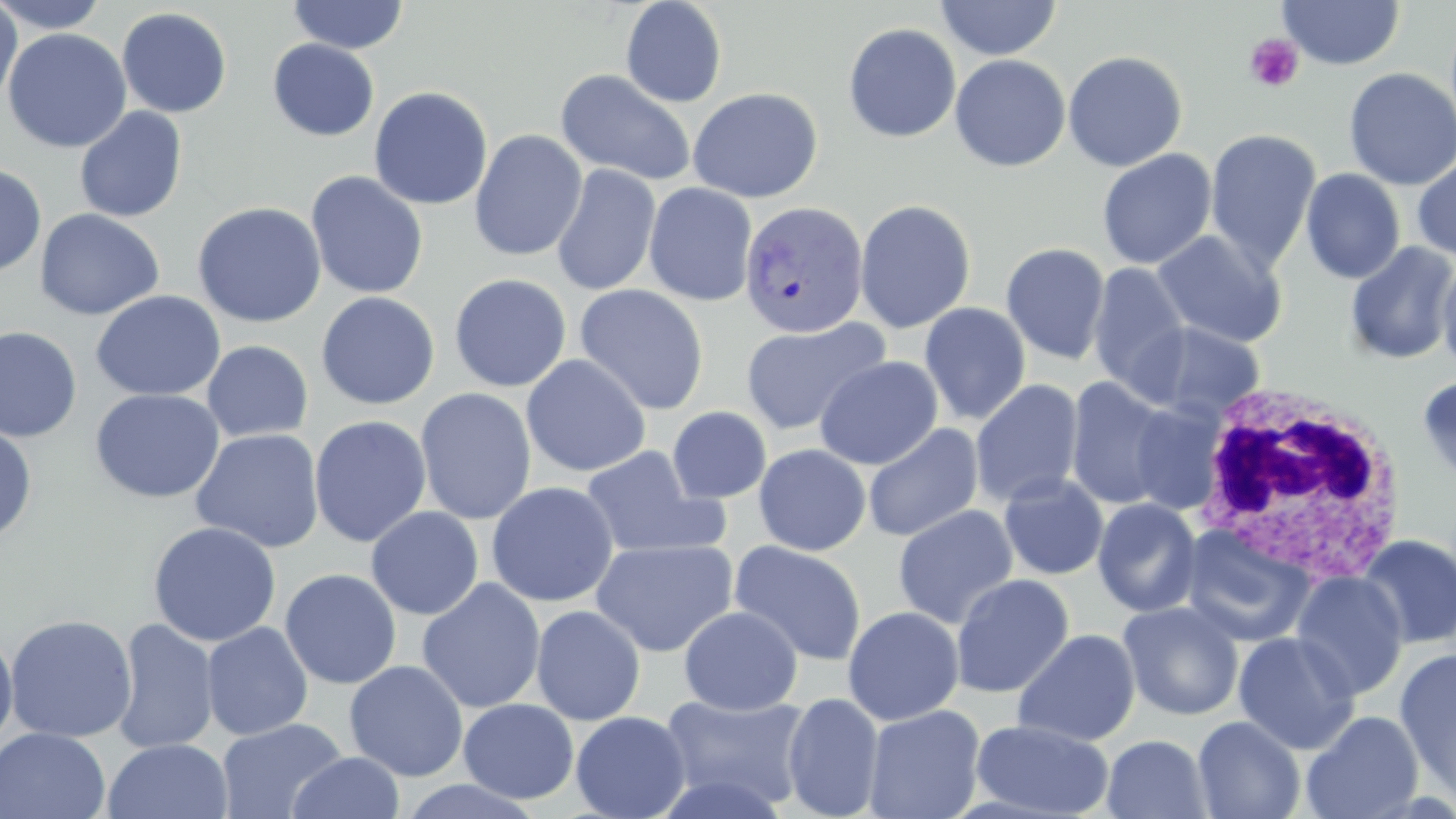

slide-level diagnosis = Plasmodium vivax
magnification = 1000x
image size = 1456×819 pixels
field of view = one of a larger specimen
white blood cell locations = approximate bounding boxes as (x1, y1, x2, y2) in pixels: (1189, 383, 1411, 580)
modality = light microscopy
Plasmodium vivax-infected red blood cell locations = approximate bounding boxes as (x1, y1, x2, y2) in pixels: (740, 202, 870, 339)
stain = May-Grünwald-Giemsa
platelet locations = approximate bounding boxes as (x1, y1, x2, y2) in pixels: (1244, 33, 1304, 93)
uninfected red blood cell locations = approximate bounding boxes as (x1, y1, x2, y2) in pixels: (0, 0, 110, 34), (287, 0, 409, 54), (620, 0, 727, 108), (1277, 0, 1405, 70), (935, 1, 1062, 60), (0, 2, 22, 110), (116, 7, 232, 118), (842, 23, 961, 143), (2, 28, 132, 153), (267, 39, 380, 141), (1063, 50, 1188, 172), (950, 54, 1071, 173), (1343, 67, 1456, 190), (555, 69, 697, 187), (369, 86, 493, 210), (687, 87, 823, 203), (74, 107, 188, 223), (1205, 128, 1321, 271), (469, 129, 588, 261), (1097, 149, 1217, 269), (1412, 154, 1456, 261), (0, 161, 47, 278), (551, 164, 661, 297), (1300, 169, 1405, 284), (305, 170, 429, 300), (643, 182, 757, 306), (854, 199, 976, 334), (192, 201, 327, 328), (34, 208, 164, 320), (1152, 230, 1288, 348), (1000, 242, 1111, 364), (1346, 242, 1456, 365), (1437, 254, 1456, 378), (1088, 263, 1190, 396), (449, 273, 572, 392), (574, 284, 709, 415), (90, 290, 226, 402), (316, 291, 440, 410), (919, 302, 1031, 425), (740, 317, 890, 435), (1133, 321, 1266, 421), (0, 325, 82, 443), (201, 340, 314, 443), (520, 354, 651, 477), (814, 355, 943, 470), (1416, 374, 1456, 486), (1066, 377, 1179, 510), (970, 379, 1084, 508), (415, 387, 537, 525), (90, 388, 225, 503), (1129, 402, 1226, 513), (667, 406, 772, 504), (309, 415, 432, 548), (862, 423, 983, 542), (0, 424, 38, 545), (191, 428, 325, 553), (753, 443, 871, 556), (579, 444, 726, 560), (998, 473, 1109, 580), (485, 482, 619, 607), (1093, 497, 1203, 618), (892, 505, 1019, 629), (365, 506, 484, 620), (147, 521, 282, 647), (1180, 523, 1316, 648), (1356, 535, 1456, 649), (590, 537, 739, 657), (729, 540, 867, 666), (280, 568, 402, 689), (1290, 571, 1409, 701), (951, 573, 1074, 698), (417, 578, 546, 714), (1118, 601, 1244, 720), (530, 605, 646, 726), (678, 605, 802, 715), (842, 606, 965, 726), (4, 614, 138, 744), (111, 618, 219, 754), (201, 622, 313, 740), (0, 628, 18, 752), (1012, 629, 1140, 746), (1232, 632, 1361, 754), (1395, 647, 1456, 798), (344, 660, 469, 781), (658, 691, 813, 813), (782, 693, 885, 818), (458, 698, 580, 804), (863, 704, 986, 819), (1301, 710, 1424, 819), (570, 711, 691, 819), (1193, 715, 1305, 819), (216, 717, 348, 819), (970, 719, 1114, 817), (0, 727, 111, 819), (1102, 734, 1213, 819), (103, 738, 232, 819), (286, 752, 405, 818)
preparation = thin blood smear